Identify the parasite.
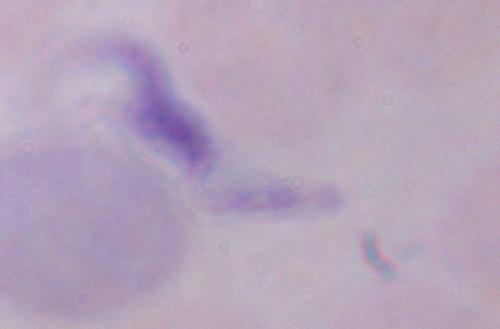

This is a trypanosome.

modality = photomicrograph
magnification = 1000x